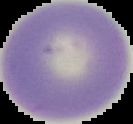

Image is 133×124 pixels. Segmented cell region on a black background. Malaria status: uninfected. From a thin blood smear.